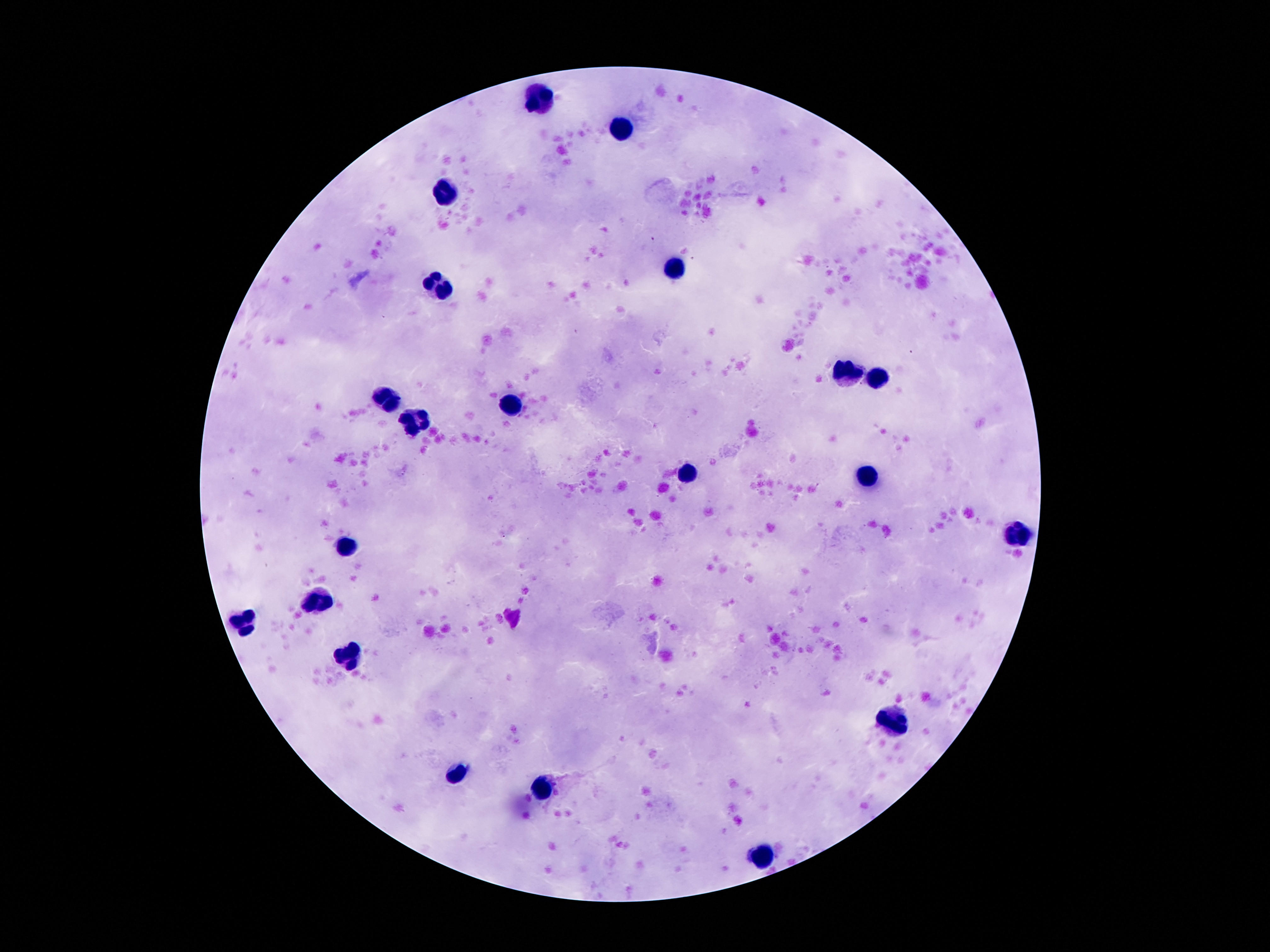
Approximate object centers, in pixels from the top-left corner. Leukocyte locations: (x=538, y=94), (x=622, y=128), (x=443, y=194), (x=674, y=269), (x=438, y=287), (x=853, y=371), (x=881, y=376), (x=390, y=400), (x=508, y=403), (x=416, y=422), (x=688, y=473), (x=869, y=478), (x=1017, y=532), (x=347, y=546), (x=320, y=600), (x=247, y=622), (x=345, y=653), (x=894, y=718), (x=458, y=775), (x=545, y=791), (x=763, y=853). Giemsa-stained preparation. 100x magnification. Patient malaria status: uninfected. Image is 1270×952 pixels. Thick blood film. Photographed through the microscope eyepiece with a smartphone camera. Single field of view.